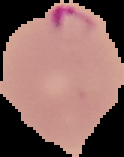 Image is 124×157 pixels. The area outside the segmented cell region is set to black. From a thin blood film. Result: Plasmodium parasites identified.